Classify this cell by malaria status.
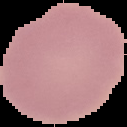
Uninfected.

The area outside the segmented cell region is set to black. Image is 127×127 pixels. From a thin blood smear.